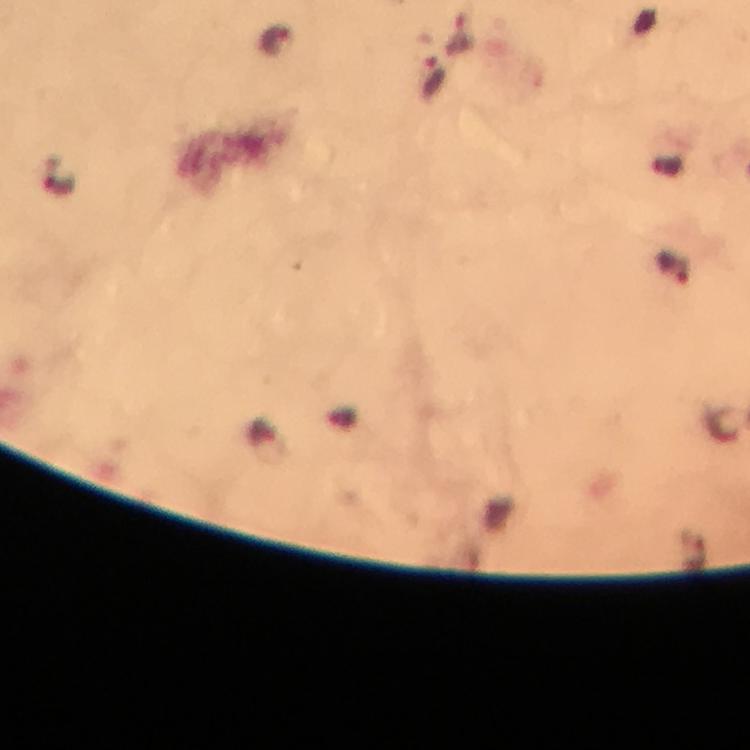 Approximate object centers, in pixels from the top-left corner. Plasmodium parasite locations: (x=461, y=35), (x=277, y=41), (x=433, y=80), (x=676, y=268). Image is 750×750 pixels. Giemsa-stained preparation. At 100x magnification. Thick blood film. Photographed with a smartphone mounted on the microscope. Cropped region of a single field of view. From a diagnostic examination for malaria. Immersion oil was used.